State the blood parasite species.
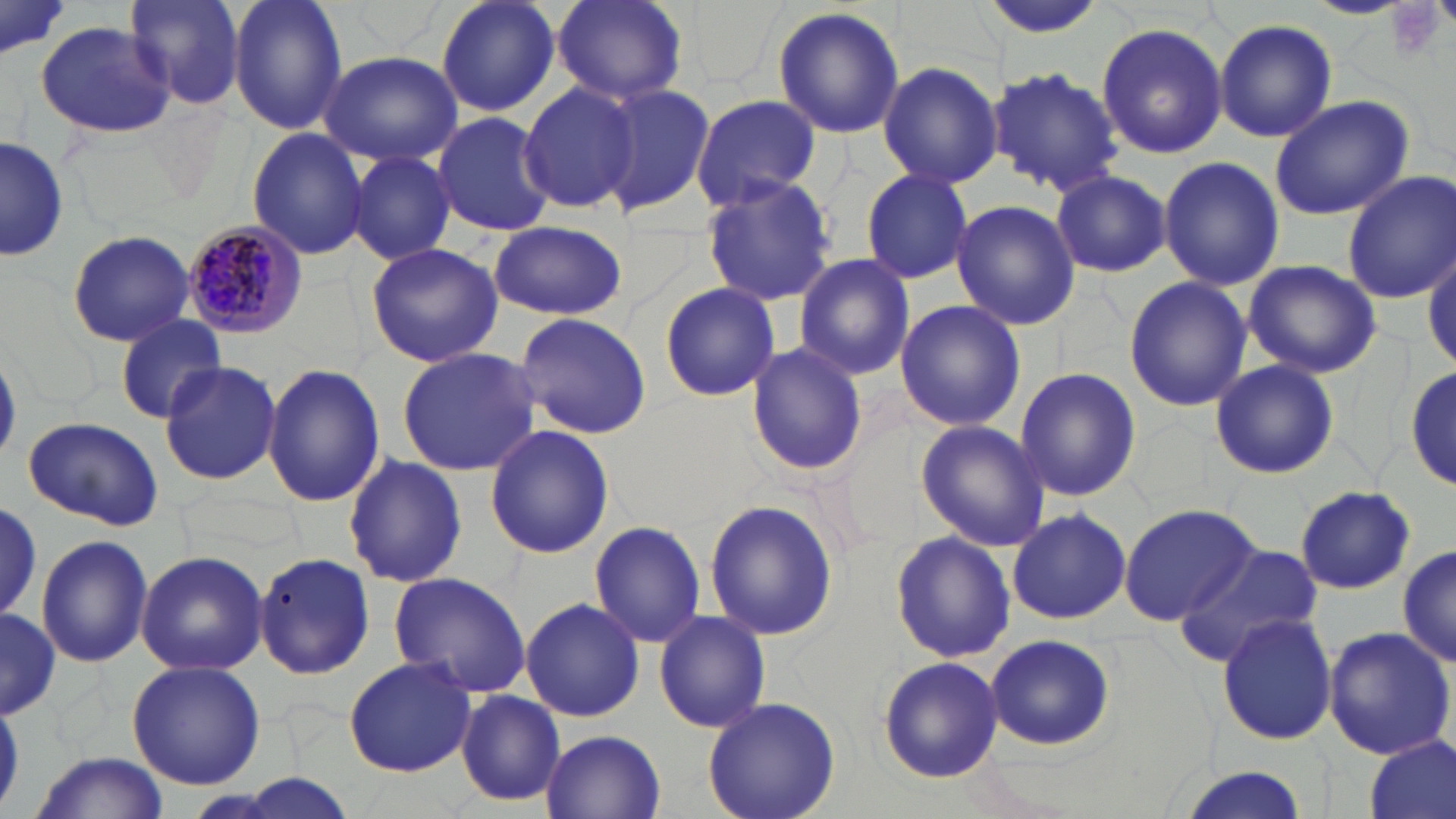
Plasmodium malariae.

Summary:
  - Coordinate format: approximate bounding boxes as (x1,y1)-(x2,y2) corner pairs in pixels
  - Plasmodium malariae-infected red blood cell locations: (180,219)-(309,340)
  - Uninfected red blood cell locations: (121,0)-(245,111), (227,0)-(348,137), (436,0)-(560,119), (551,0)-(688,108), (0,1)-(70,67), (772,7)-(906,141), (1213,19)-(1339,142), (1096,21)-(1228,158), (36,22)-(174,138), (319,48)-(464,166), (877,60)-(1002,189), (990,66)-(1124,196), (517,83)-(638,212), (595,85)-(715,215), (691,94)-(820,210), (1268,95)-(1412,221), (432,112)-(557,237), (246,127)-(370,261), (0,136)-(69,262), (347,150)-(455,265), (1158,156)-(1284,289), (860,169)-(974,285), (1051,170)-(1171,275), (1342,171)-(1456,303), (700,176)-(837,306), (950,200)-(1080,329), (487,222)-(627,321), (67,229)-(194,347), (365,242)-(505,369), (1423,242)-(1455,377), (794,253)-(916,380), (1244,259)-(1383,377), (1123,276)-(1252,413), (660,281)-(780,402), (893,299)-(1026,432), (513,314)-(652,438), (115,317)-(228,422), (745,342)-(868,477), (397,346)-(541,475), (159,359)-(283,486), (1209,359)-(1340,481), (1406,359)-(1455,493), (261,362)-(386,508), (1014,367)-(1141,503), (22,416)-(165,531), (916,422)-(1050,549), (484,425)-(613,559), (343,455)-(468,589), (1294,485)-(1416,594), (703,497)-(840,642), (0,501)-(46,624), (1118,502)-(1262,627), (1006,507)-(1133,624), (588,521)-(706,648), (889,531)-(1016,664), (36,535)-(153,668), (1397,539)-(1454,670), (1171,542)-(1323,668), (136,551)-(267,676), (255,551)-(376,681), (389,571)-(532,699), (520,597)-(645,722), (0,606)-(57,722), (654,610)-(772,735), (1217,613)-(1339,745), (1321,626)-(1454,761), (983,633)-(1116,750), (878,655)-(1002,782), (342,656)-(478,777), (126,660)-(265,791), (454,690)-(567,809), (701,697)-(842,819), (541,730)-(666,817), (1363,735)-(1454,819), (30,753)-(168,819), (1171,767)-(1314,819), (206,777)-(363,818)
  - Platelet locations: (1387,2)-(1449,61)
  - Stain: May-Grünwald-Giemsa
  - Magnification: 1000x
  - Modality: light microscopy
  - Image size: 1456×819 pixels
  - Field of view: one of a larger specimen
  - Preparation: thin blood film